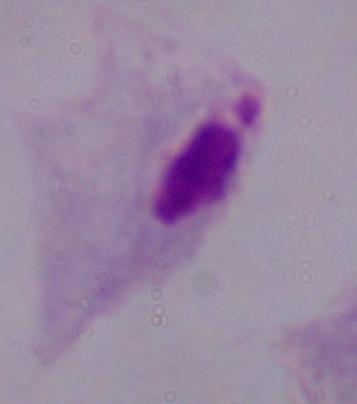

modality: photomicrograph
magnification: 1000x
identification: trichomonad